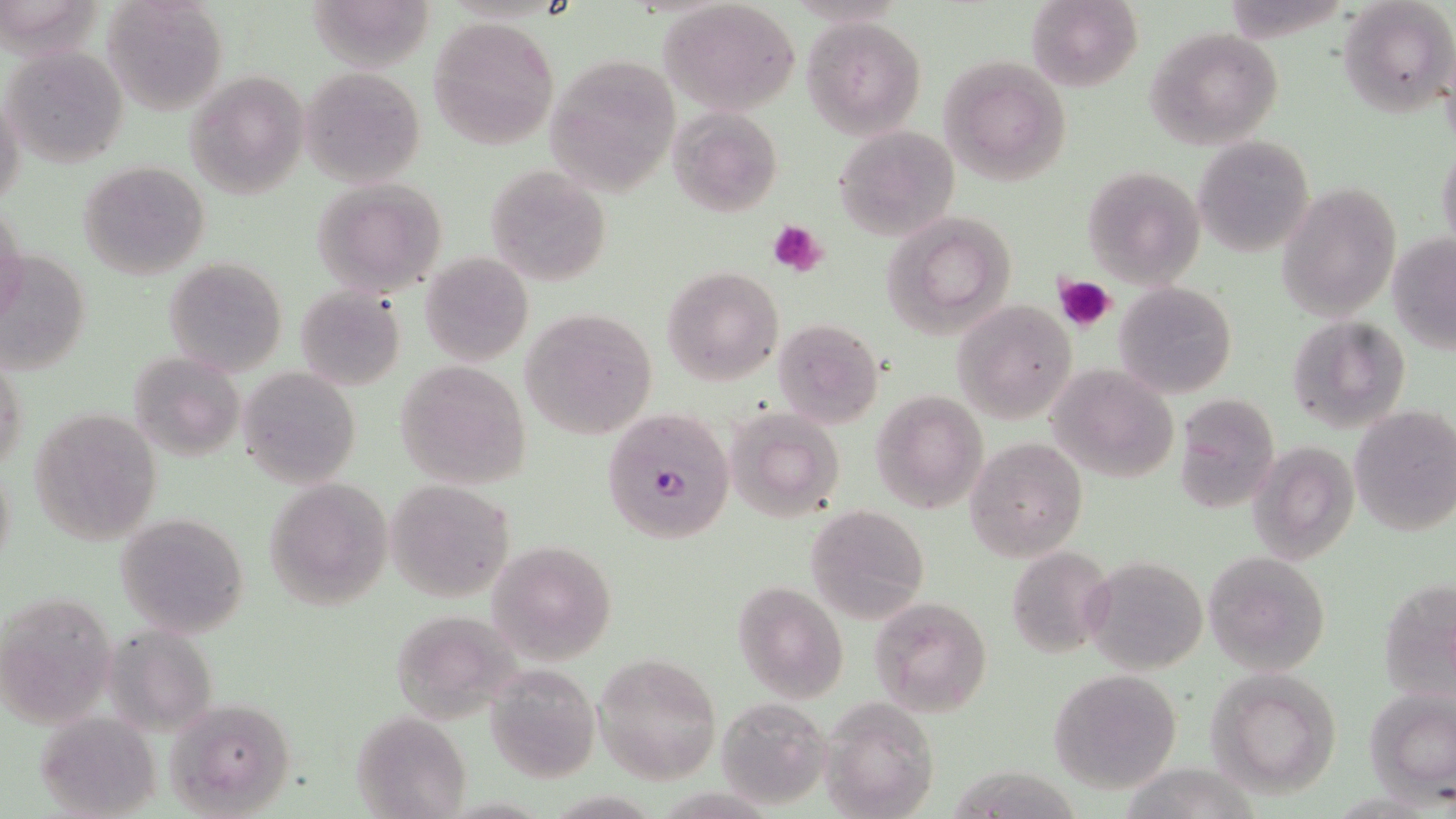
slide-level diagnosis = Plasmodium falciparum
platelet locations = approximate bounding boxes as (x1,y1)-(x2,y2) corner pairs in pixels: (769,220)-(830,277), (1053,274)-(1116,333)
preparation = thin blood film
uninfected red blood cell locations = approximate bounding boxes as (x1,y1)-(x2,y2) corner pairs in pixels: (102,0)-(228,117), (1026,0)-(1144,93), (1339,0)-(1454,118), (0,1)-(118,63), (659,1)-(802,114), (303,4)-(440,78), (802,16)-(926,137), (428,17)-(558,148), (1144,28)-(1283,150), (1,46)-(129,168), (542,55)-(680,195), (939,55)-(1072,185), (301,66)-(425,188), (184,71)-(309,200), (1,90)-(25,214), (667,107)-(783,219), (834,125)-(958,240), (1193,135)-(1314,258), (1436,147)-(1456,258), (78,161)-(209,280), (486,164)-(612,288), (1082,165)-(1205,287), (310,179)-(448,298), (1275,182)-(1401,322), (0,201)-(26,321), (880,211)-(1021,338), (1388,233)-(1456,352), (1,251)-(92,375), (420,252)-(534,367), (163,257)-(289,376), (660,266)-(784,385), (1115,281)-(1238,398), (295,286)-(405,391), (951,300)-(1078,423), (521,308)-(657,439), (1285,315)-(1411,437), (772,317)-(885,429), (128,350)-(246,461), (1,353)-(29,481), (394,362)-(532,489), (1047,364)-(1178,484), (239,366)-(361,491), (871,391)-(988,514), (1175,395)-(1281,514), (29,406)-(163,545), (725,407)-(845,525), (1350,407)-(1456,538), (965,437)-(1087,561), (1247,440)-(1359,565), (1,455)-(15,578), (264,476)-(395,611), (386,478)-(515,602), (805,505)-(929,622), (114,511)-(252,638), (488,538)-(617,664), (1005,545)-(1117,657), (1201,550)-(1331,677), (1085,556)-(1206,674), (1378,578)-(1455,705), (732,581)-(848,702), (2,589)-(118,727), (870,595)-(993,716), (391,611)-(528,721), (99,623)-(216,739), (595,652)-(723,783), (483,665)-(599,784), (1205,668)-(1345,800), (1048,669)-(1184,792), (1364,687)-(1456,801), (165,697)-(298,817), (821,697)-(941,818), (716,698)-(833,809), (33,711)-(161,819), (351,712)-(471,817), (957,763)-(1099,819)
image size = 1456×819 pixels
Plasmodium falciparum-infected red blood cell locations = approximate bounding boxes as (x1,y1)-(x2,y2) corner pairs in pixels: (600,409)-(736,545)
stain = May-Grünwald-Giemsa
field of view = one of a larger specimen
modality = light microscopy
magnification = 1000x